Assess this cell for malaria.
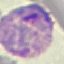

Parasitized.

Acquired by smartphone through the microscope eyepiece. Giemsa stain. Cell patch, automatically extracted from a larger field of view and resized to 64 × 64 pixels. Thin blood film.